State the blood parasite species.
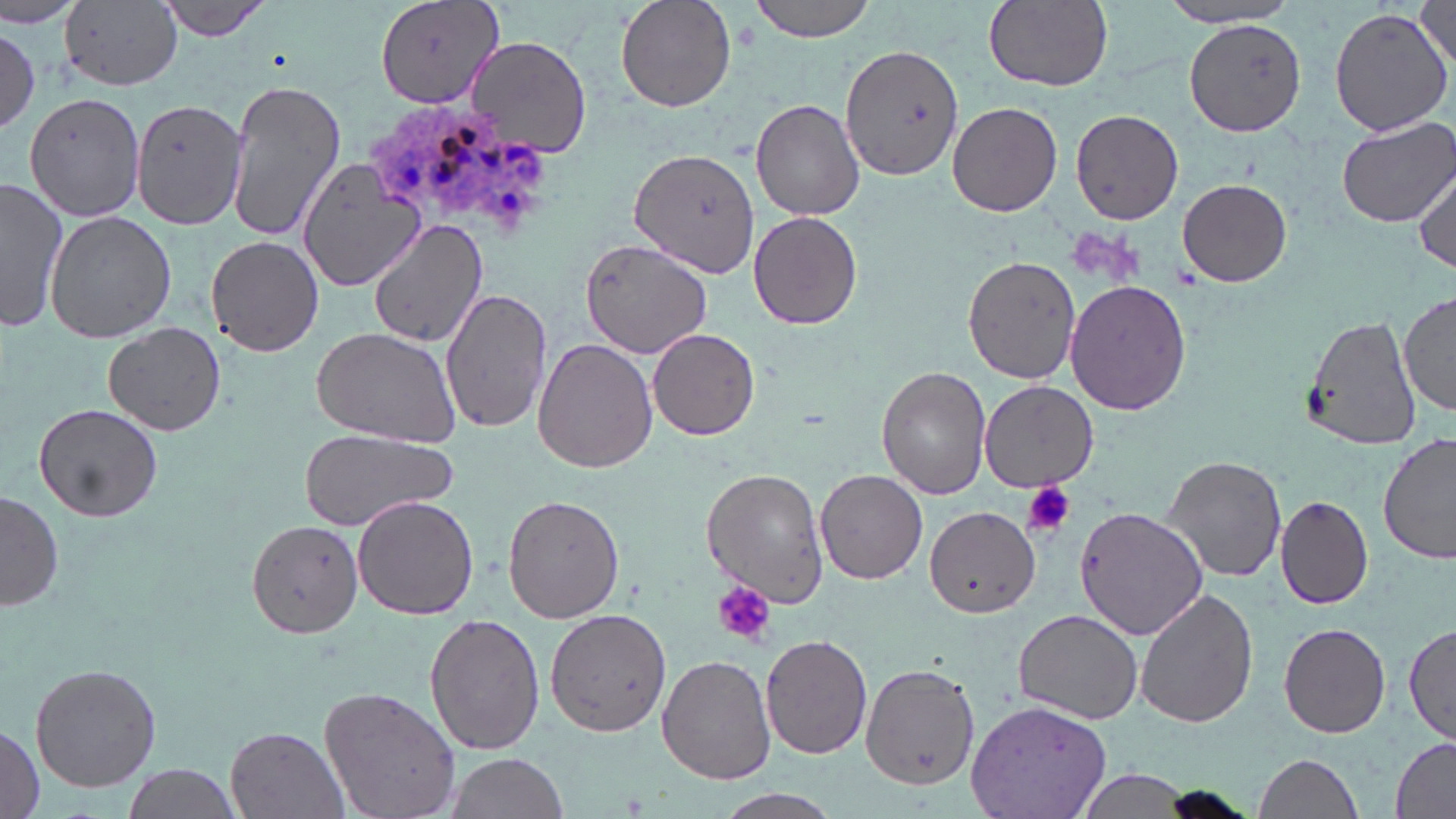

Plasmodium ovale.

Approximate bounding boxes as [x1, y1, x2, y2] in pixels. Plasmodium ovale-infected red blood cell locations: [364, 105, 554, 237]. Platelet locations: [735, 16, 760, 52], [1022, 481, 1075, 537], [714, 581, 775, 645]. Uninfected red blood cell locations: [1, 0, 90, 27], [153, 0, 276, 41], [373, 0, 503, 112], [616, 0, 737, 113], [748, 0, 880, 41], [982, 0, 1113, 90], [61, 1, 185, 90], [1154, 2, 1304, 28], [1413, 3, 1455, 71], [1327, 7, 1452, 138], [1183, 17, 1307, 135], [0, 27, 42, 136], [465, 35, 592, 158], [843, 40, 963, 178], [223, 78, 346, 245], [24, 93, 148, 221], [751, 98, 866, 220], [132, 100, 246, 229], [949, 100, 1063, 216], [1071, 108, 1183, 224], [1335, 116, 1456, 228], [631, 149, 762, 280], [295, 158, 423, 292], [1414, 163, 1455, 272], [1177, 178, 1293, 287], [0, 179, 69, 332], [46, 210, 177, 343], [748, 210, 864, 330], [369, 217, 487, 349], [206, 236, 325, 355], [580, 237, 714, 358], [964, 255, 1083, 385], [1065, 278, 1194, 416], [441, 287, 553, 433], [1399, 290, 1455, 417], [1301, 315, 1420, 451], [103, 321, 225, 436], [310, 326, 462, 446], [647, 327, 760, 439], [532, 338, 658, 472], [876, 366, 992, 500], [979, 382, 1101, 493], [34, 402, 163, 523], [298, 427, 456, 532], [1378, 432, 1454, 565], [1161, 455, 1287, 582], [704, 468, 830, 606], [816, 470, 927, 583], [1, 489, 64, 611], [1275, 494, 1373, 608], [353, 496, 479, 621], [503, 496, 622, 623], [924, 506, 1041, 618], [1072, 506, 1207, 640], [245, 517, 364, 639], [1134, 587, 1258, 728], [1014, 608, 1142, 724], [545, 609, 672, 738], [424, 613, 545, 756], [1279, 621, 1391, 738], [1401, 622, 1456, 744], [760, 634, 873, 759], [658, 654, 775, 784], [33, 660, 163, 791], [860, 660, 980, 789], [318, 684, 461, 819], [968, 698, 1113, 819], [0, 724, 43, 819], [227, 727, 347, 818], [1390, 736, 1456, 817], [445, 752, 567, 819], [1252, 753, 1368, 819], [118, 763, 246, 819], [1068, 771, 1207, 817], [1153, 786, 1256, 819], [711, 789, 844, 819]. Captured at 1000x magnification. Thin blood smear. May-Grünwald-Giemsa-stained preparation. Single field of view. Optical microscopy. Image is 1456×819 pixels.